Name the parasite shown.
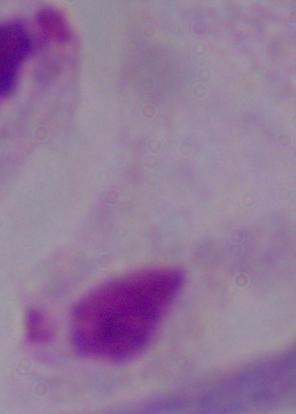
A trichomonad.

Summary:
  - Magnification: 1000x
  - Modality: micrograph